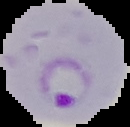 Result: malaria parasites identified. Image is 130×127 pixels. The area outside the segmented cell region is set to black. From a thin blood film.